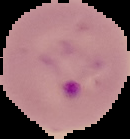

preparation = thin blood smear
result = Plasmodium parasites detected
image size = 130×139 pixels
image type = segmented cell region on a black background